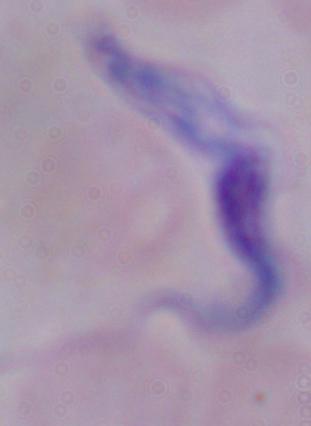

1000x magnification. A trypanosome is shown. Photomicrograph.